Classify this cell by malaria status.
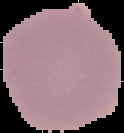
It is uninfected.

From a thin blood smear. Image is 124×133 pixels. Segmented cell region on a black background.